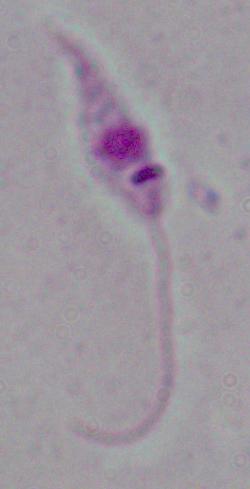

Summary:
  - Modality: micrograph
  - Identification: Leishmania
  - Magnification: 1000x